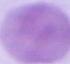
An erythrocyte is seen. Photomicrograph. Captured at 1000x magnification.